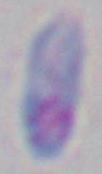 Toxoplasma gondii is seen. Photomicrograph. Captured at 1000x magnification.